Classify this cell by malaria status.
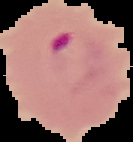
It is parasitized.

Segmented cell region on a black background. From a thin blood smear. Image is 133×142 pixels.